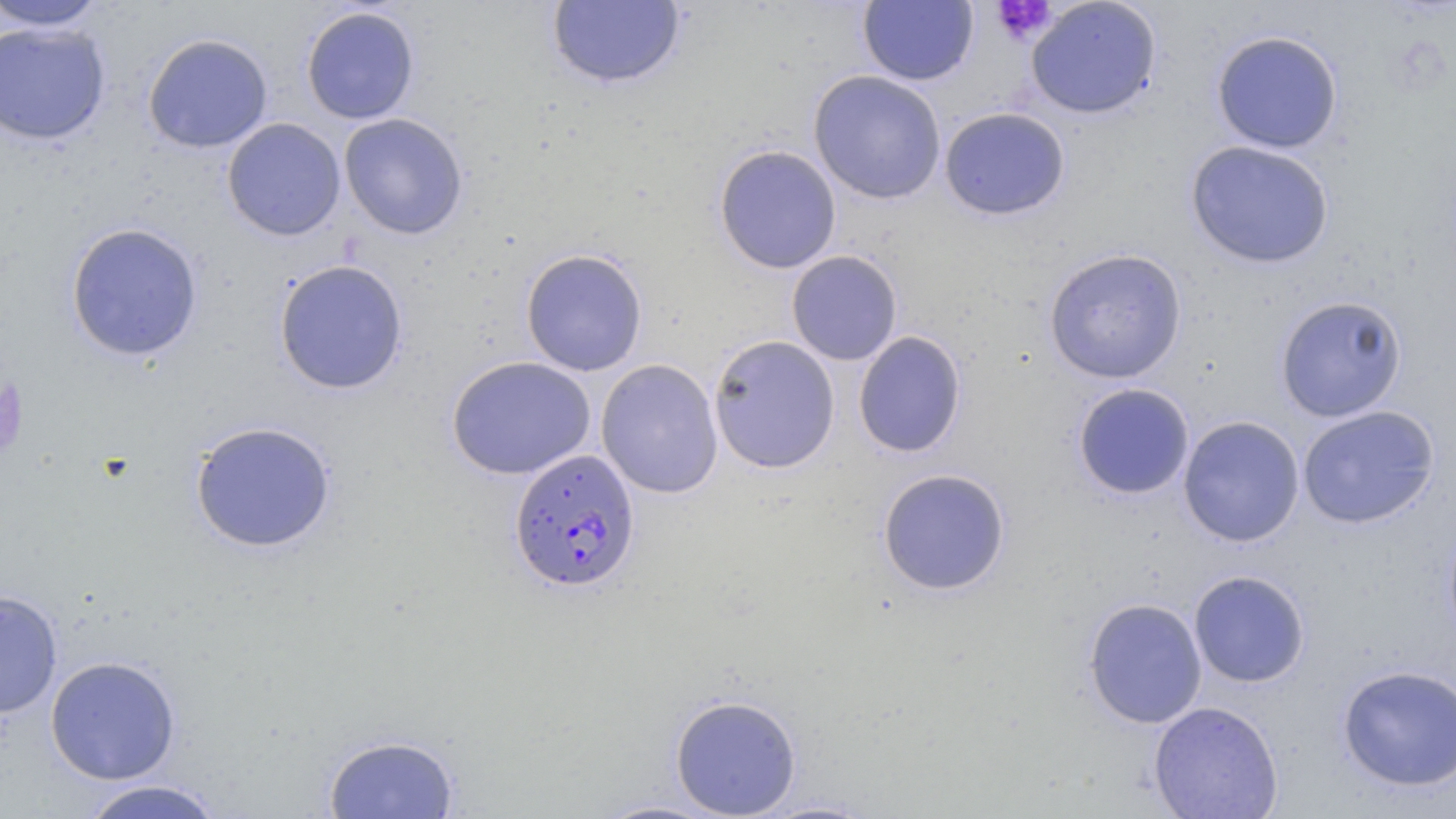 Approximate bounding boxes as (x1,y1)-(x2,y2) corner pairs in pixels. Plasmodium falciparum-infected red blood cell locations: (508,448)-(642,593). Uninfected red blood cell locations: (546,0)-(686,90), (858,0)-(978,86), (1026,0)-(1162,120), (0,1)-(110,31), (300,6)-(420,124), (0,22)-(111,145), (1211,30)-(1344,154), (142,33)-(273,153), (808,70)-(947,205), (939,107)-(1071,221), (338,113)-(469,240), (222,118)-(346,242), (1185,140)-(1335,269), (713,144)-(842,274), (64,222)-(204,362), (1043,247)-(1187,384), (520,248)-(648,376), (786,250)-(903,366), (273,259)-(409,395), (1274,295)-(1408,422), (853,330)-(967,458), (708,335)-(840,473), (446,356)-(596,480), (596,359)-(724,499), (1072,383)-(1194,500), (1297,404)-(1439,529), (1177,416)-(1304,547), (189,420)-(337,553), (876,468)-(1011,597), (1442,514)-(1456,650), (1188,570)-(1310,688), (0,589)-(63,719), (1082,597)-(1208,729), (45,655)-(181,784), (1337,664)-(1456,792), (669,693)-(802,818), (1148,701)-(1283,819), (323,732)-(460,818), (76,779)-(227,819), (587,798)-(728,818), (753,799)-(879,818). Platelet locations: (990,1)-(1057,43). Slide-level diagnosis: Plasmodium falciparum. One field of a larger specimen. 1000x magnification. Image is 1456×819 pixels. Thin blood film. May-Grünwald-Giemsa stain. Optical microscopy.